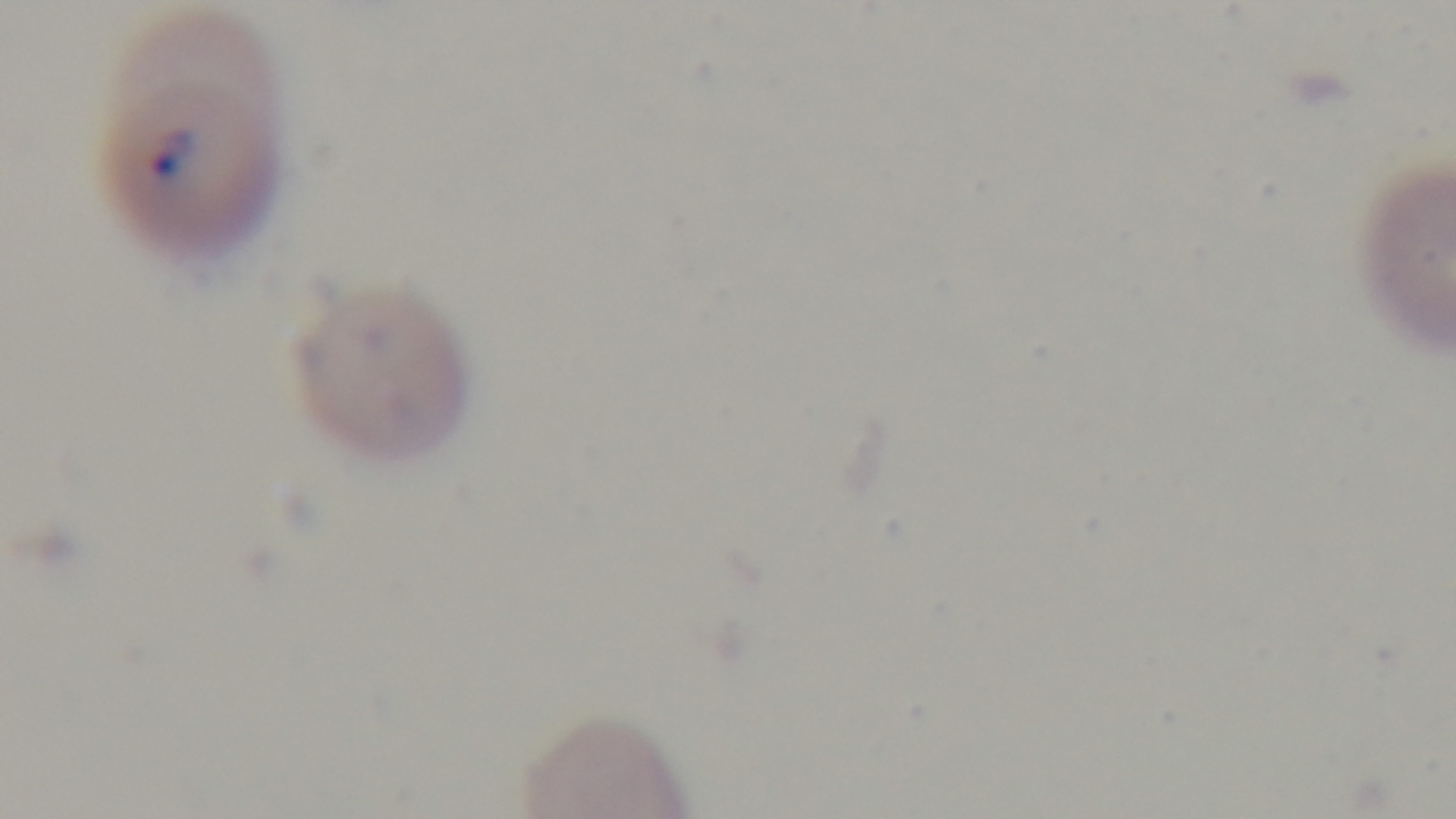
Preparation: thin smear. Photomicrograph. Giemsa-stained. One field from the slide. Malaria status: positive. 100x oil-immersion objective. Captured with a mounted 4K digital camera.